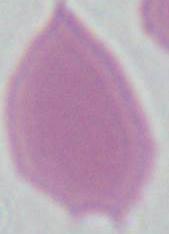
magnification = 1000x
identification = red blood cell
modality = micrograph